Assess this cell for malaria.
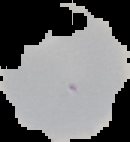

It is uninfected.

From a thin blood film. Image is 130×142 pixels. Cell region segmented out of the field of view; the surrounding area is masked to black.